Outline each uninfected red blood cell.
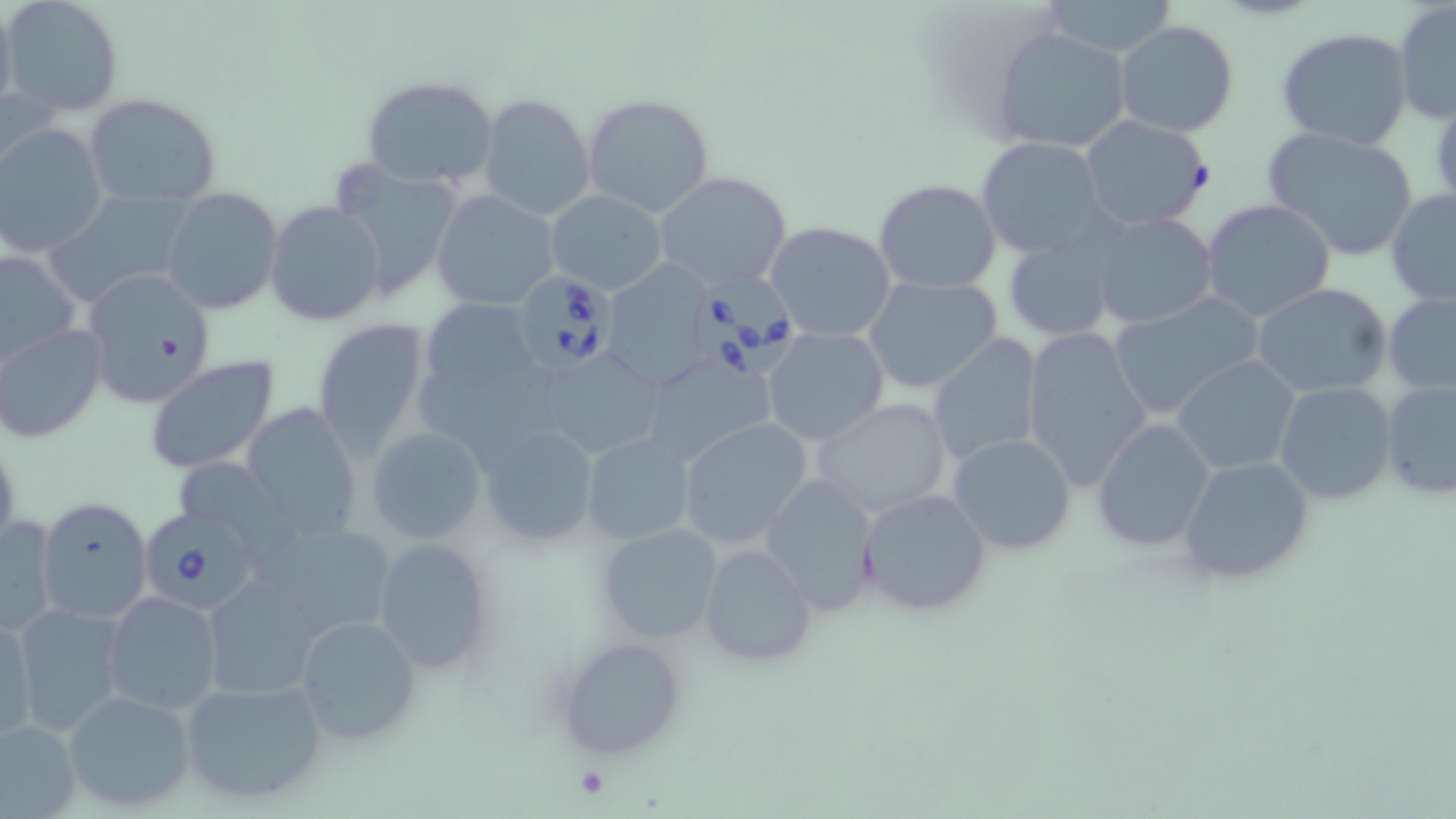
Approximate bounding boxes as (x1,y1)-(x2,y2) corner pairs in pixels.
Uninfected red blood cells: (0,0)-(17,118), (3,0)-(124,117), (1041,0)-(1182,58), (1393,3)-(1455,125), (1112,19)-(1240,137), (1276,28)-(1415,152), (995,29)-(1130,154), (359,74)-(498,190), (582,93)-(715,219), (83,94)-(224,207), (479,94)-(595,222), (1080,114)-(1213,232), (0,124)-(107,257), (1261,124)-(1422,262), (976,137)-(1109,258), (329,160)-(463,302), (652,171)-(793,295), (874,178)-(1002,294), (160,187)-(284,314), (1385,189)-(1456,307), (431,190)-(561,310), (545,190)-(668,295), (46,192)-(192,305), (1200,197)-(1336,322), (267,201)-(388,327), (1088,212)-(1218,331), (763,221)-(896,342), (1002,233)-(1120,341), (0,249)-(80,365), (599,263)-(721,393), (80,271)-(214,407), (861,273)-(1004,395), (1252,282)-(1393,401), (1384,292)-(1456,396), (1109,293)-(1265,420), (418,295)-(545,405), (312,318)-(431,460), (0,324)-(107,443), (1021,326)-(1152,491), (763,327)-(888,447), (930,334)-(1044,467), (534,346)-(662,459), (637,351)-(780,471), (1172,355)-(1301,476), (145,357)-(279,474), (1381,379)-(1456,499), (1274,380)-(1398,505), (811,397)-(956,520), (242,403)-(363,541), (676,416)-(814,550), (1093,418)-(1216,553), (475,424)-(603,554), (366,426)-(488,547), (581,432)-(697,547), (948,433)-(1077,555), (1177,455)-(1318,588), (171,456)-(287,548), (761,475)-(881,617), (857,488)-(992,617), (37,496)-(153,623), (1,512)-(62,638), (255,517)-(397,645), (594,523)-(723,643), (372,538)-(496,676), (697,543)-(816,668), (199,576)-(326,702), (102,591)-(226,715), (8,603)-(128,736), (0,609)-(37,743), (290,612)-(421,749), (557,636)-(687,762), (178,675)-(329,808), (63,689)-(199,813), (0,719)-(81,816).

Summary:
  - Babesia divergens-infected red blood cell locations: (694,268)-(809,383), (512,272)-(617,372), (140,508)-(261,613)
  - Platelet locations: (576,767)-(612,798)
  - Slide-level diagnosis: Babesia divergens
  - Field of view: single
  - Preparation: thin blood film
  - Image size: 1456×819 pixels
  - Stain: May-Grünwald-Giemsa
  - Modality: light microscopy
  - Magnification: 1000x